Give the position of every Plasmodium parasite visible.
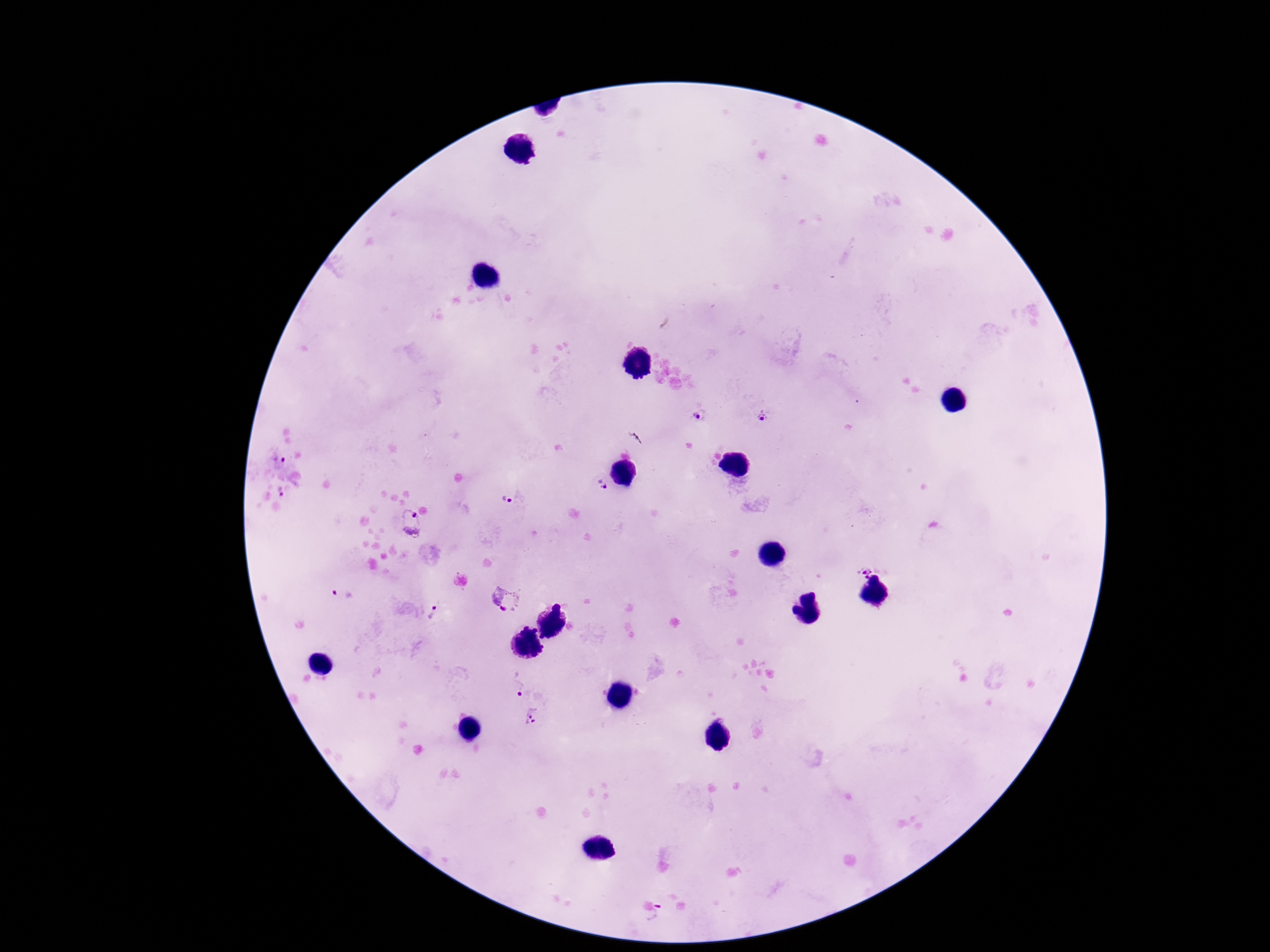
Approximate centers as {x, y} in pixels.
Plasmodium parasites: {698, 416}, {764, 416}, {601, 485}, {279, 493}, {508, 500}, {410, 514}, {411, 534}, {866, 571}, {343, 593}, {505, 599}, {434, 612}, {518, 685}, {532, 716}, {658, 914}.

Summary:
  - Patient malaria status: positive
  - Capture: smartphone camera through the microscope eyepiece
  - Stain: Giemsa
  - Magnification: 100x
  - Field of view: single
  - Preparation: thick peripheral-blood smear
  - Image size: 1270×952 pixels